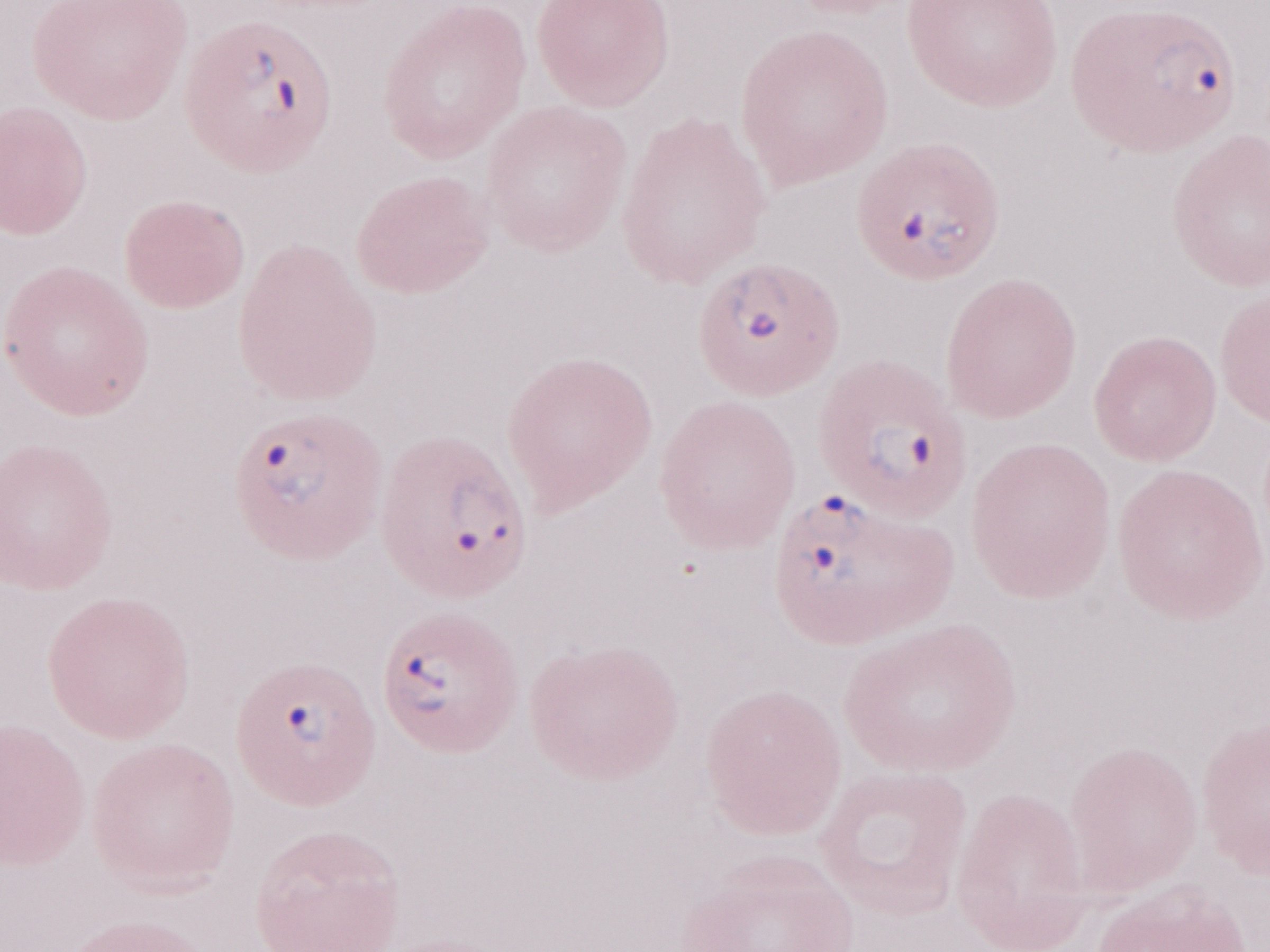 Olympus BX43 microscope, Olympus DP73 camera. Thin peripheral-blood smear. Single field of view. Image is 1270×952 pixels. 1,000x magnification. May-Grünwald-Giemsa-stained preparation. Patient-level malaria diagnosis: positive.